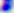
Summary:
  - Identification: Toxoplasma gondii
  - Modality: photomicrograph
  - Magnification: 400x